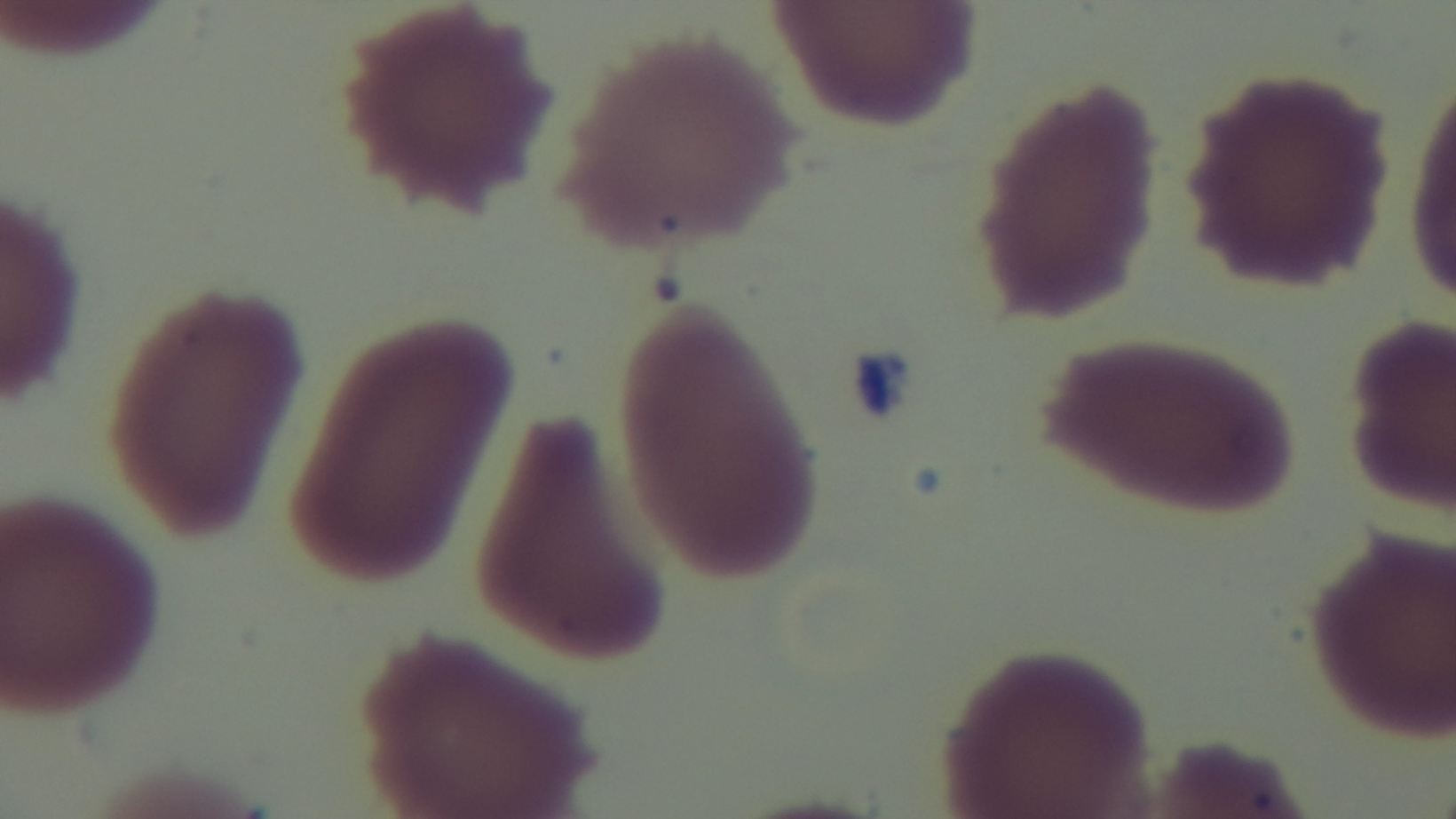

field of view = single
modality = light microscopy
objective = 100x oil immersion
stain = Giemsa
malaria status = uninfected
capture = mounted 4K digital camera
preparation = thin